Identify the parasite.
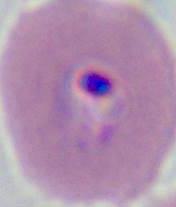
Plasmodium.

magnification = 400x or 1000x
modality = micrograph